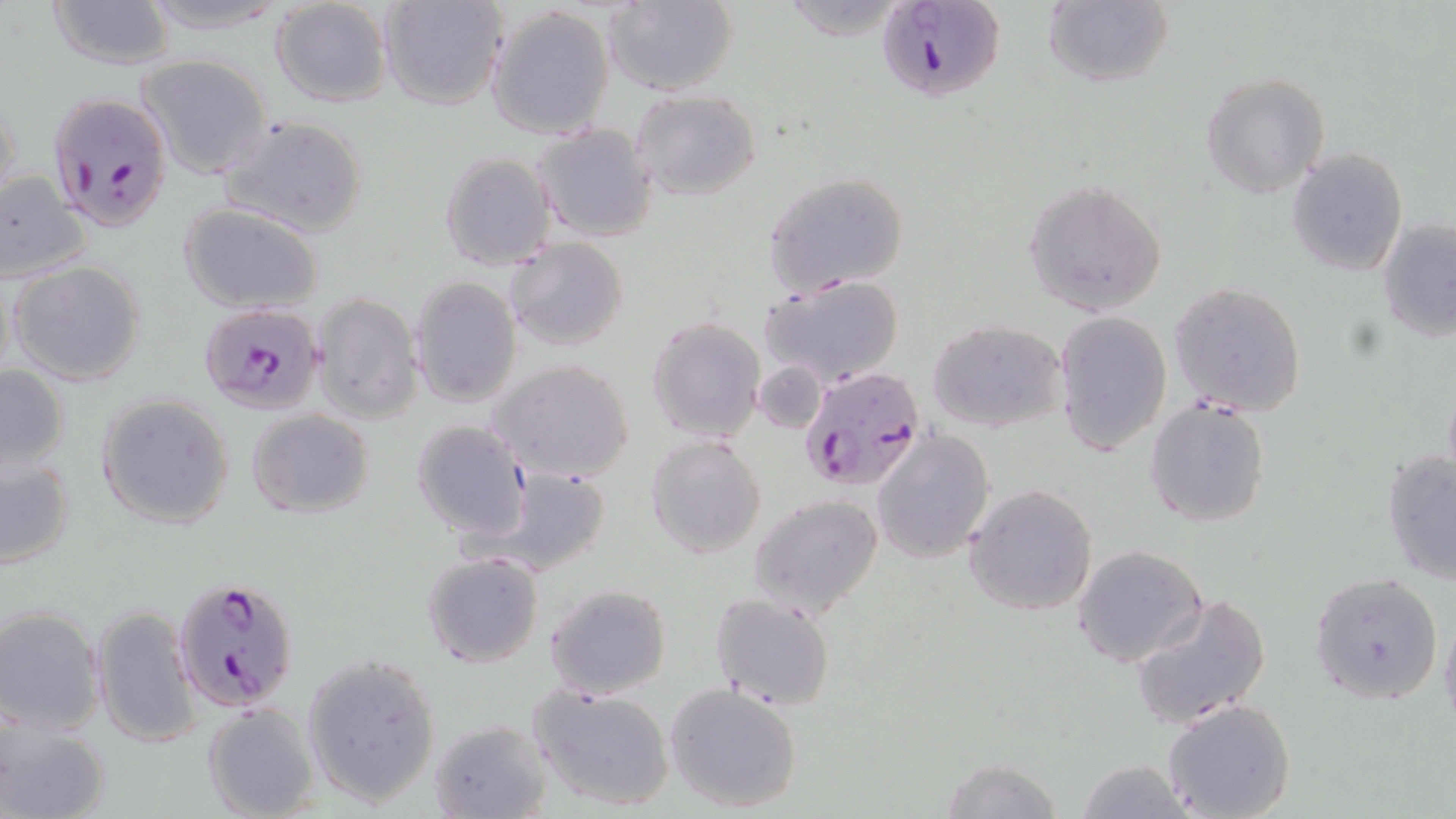

Summary:
  - Coordinate format: approximate bounding boxes as (x1, y1, x2, y2) in pixels
  - Uninfected red blood cell locations (subset): (43, 0, 176, 71), (133, 0, 291, 33), (270, 0, 395, 108), (381, 0, 509, 110), (601, 0, 738, 95), (1043, 1, 1174, 89), (486, 4, 617, 140), (137, 55, 272, 179), (1198, 71, 1330, 198), (0, 86, 22, 212), (630, 89, 762, 202), (218, 115, 369, 237), (533, 124, 659, 243), (1287, 147, 1409, 276), (439, 150, 559, 271), (0, 171, 93, 283), (763, 171, 912, 299), (1023, 179, 1168, 317), (177, 201, 325, 313), (1377, 215, 1456, 344), (504, 237, 629, 352), (9, 260, 147, 386), (757, 272, 905, 388), (409, 275, 522, 409), (1170, 282, 1308, 417), (312, 292, 423, 424), (1054, 310, 1172, 457), (645, 316, 766, 443), (927, 319, 1068, 434), (490, 358, 636, 483), (754, 360, 827, 433), (0, 365, 71, 472), (97, 394, 234, 529), (1144, 396, 1273, 526), (247, 409, 374, 519), (410, 419, 531, 540), (872, 429, 995, 563), (645, 434, 767, 560), (1, 449, 76, 570), (1379, 451, 1456, 584), (488, 466, 611, 575), (963, 485, 1099, 616), (749, 493, 884, 618), (1072, 544, 1207, 666), (421, 551, 545, 668), (1308, 572, 1445, 706), (544, 583, 671, 699), (709, 592, 836, 709), (1130, 593, 1270, 729), (90, 603, 202, 750), (0, 605, 105, 735), (303, 655, 440, 805), (665, 682, 804, 814), (530, 684, 675, 812), (1159, 697, 1298, 819), (201, 701, 320, 817), (1, 715, 110, 819), (430, 718, 552, 819), (940, 757, 1064, 819), (1075, 759, 1198, 817)
  - Plasmodium falciparum-infected red blood cell locations (subset): (873, 0, 1008, 104), (50, 92, 178, 230), (198, 304, 326, 415), (798, 364, 927, 493)
  - Slide-level diagnosis: Plasmodium falciparum
  - Stain: May-Grünwald-Giemsa
  - Magnification: 1000x
  - Field of view: single
  - Image size: 1456×819 pixels
  - Preparation: thin blood film
  - Modality: light microscopy